Evaluate for malaria.
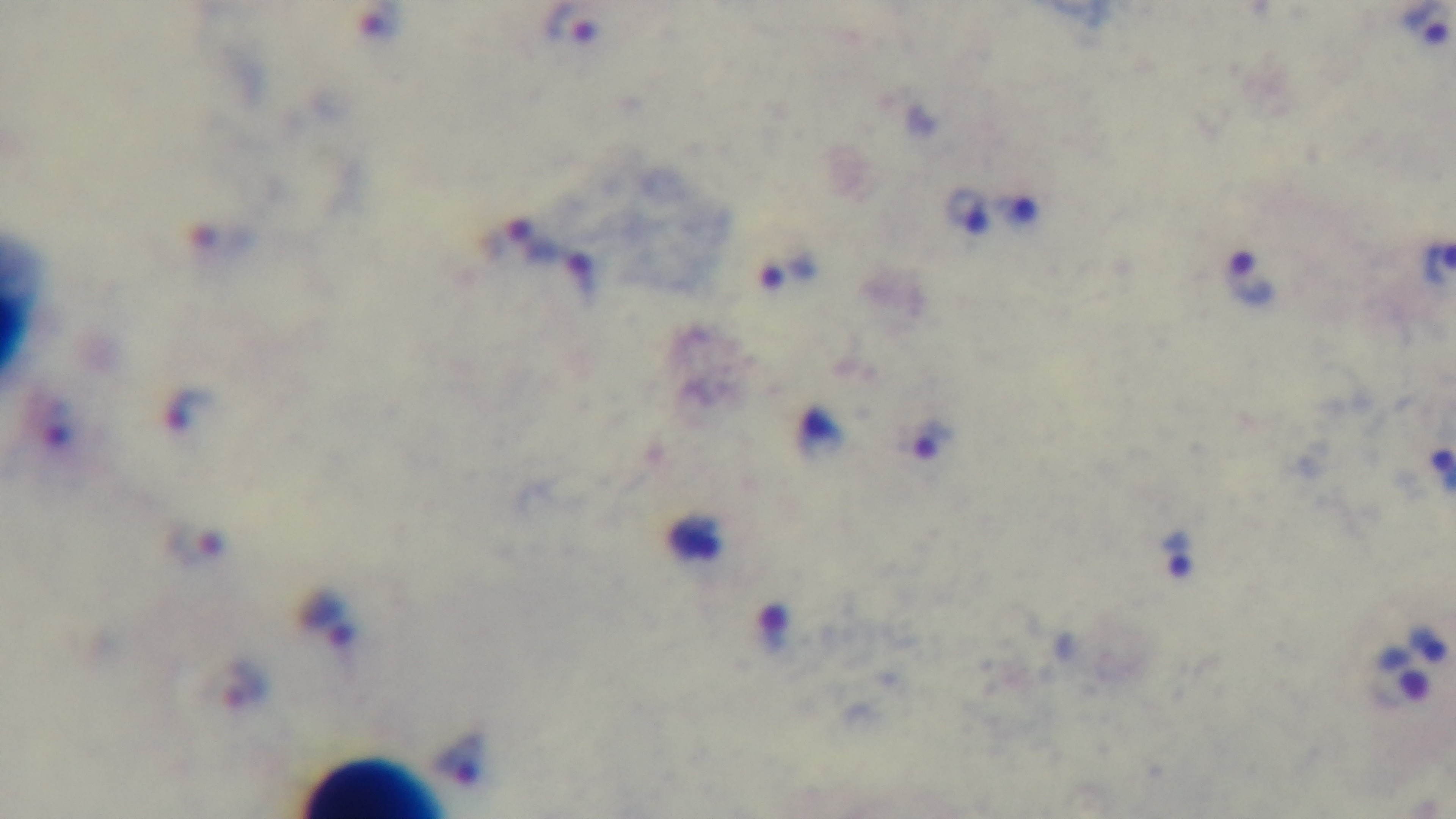

Infected.

Single field of view. Photomicrograph. Captured with a mounted 4K digital camera. Giemsa stain. 100x oil-immersion objective. Preparation: thick blood film.